State which parasite is depicted.
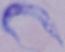
A trypanosome.

Micrograph. 1000x magnification.